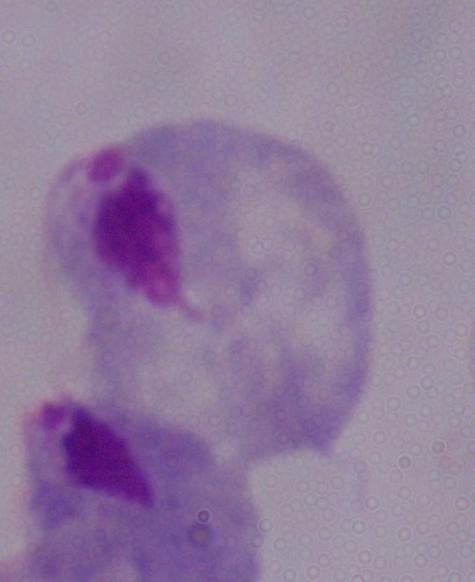 1000x magnification. A trichomonad is shown. Photomicrograph.